Classify this cell by malaria status.
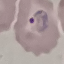

Parasitized.

Summary:
  - Capture: smartphone through the microscope eyepiece
  - Preparation: thin blood film
  - Stain: Giemsa
  - Image type: cell patch, automatically extracted from a larger field of view and resized to 64 × 64 pixels